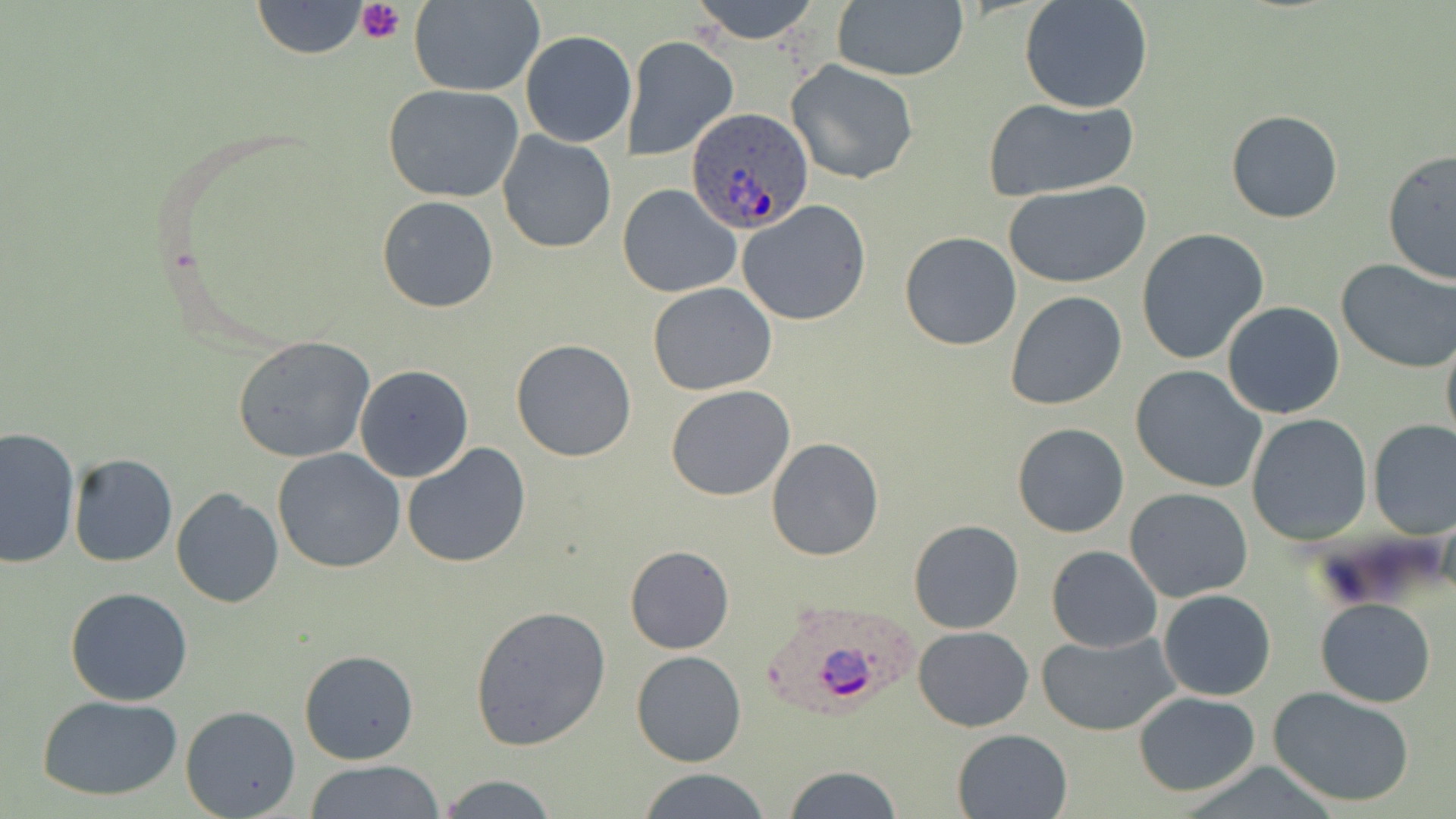

Summary:
  - Coordinate format: approximate bounding boxes as (x1,y1)-(x2,y2) corner pairs in pixels
  - Uninfected red blood cell locations: (252,0)-(369,59), (688,0)-(824,45), (830,0)-(969,82), (1019,0)-(1154,114), (409,1)-(545,96), (520,29)-(637,147), (621,37)-(738,160), (787,60)-(919,185), (382,85)-(524,204), (981,96)-(1140,201), (1226,108)-(1344,223), (496,131)-(617,255), (1382,150)-(1456,285), (1005,181)-(1150,288), (618,182)-(742,299), (376,195)-(500,313), (738,200)-(872,326), (1136,228)-(1271,365), (900,232)-(1020,351), (1336,257)-(1456,373), (648,282)-(778,394), (1004,290)-(1128,410), (1221,302)-(1345,418), (1440,333)-(1456,452), (233,336)-(374,463), (510,339)-(637,462), (354,364)-(473,481), (1131,365)-(1269,494), (665,384)-(795,501), (1245,413)-(1372,546), (1367,420)-(1455,537), (1012,423)-(1129,538), (0,426)-(80,568), (766,438)-(885,560), (402,443)-(532,569), (272,448)-(405,573), (68,454)-(178,568), (171,488)-(283,608), (1124,488)-(1254,602), (908,520)-(1024,635), (624,544)-(735,653), (1045,544)-(1162,652), (65,586)-(194,707), (1158,589)-(1276,702), (1315,599)-(1436,708), (470,604)-(612,750), (913,626)-(1034,731), (1038,631)-(1181,737), (299,648)-(420,766), (630,650)-(746,767), (1268,686)-(1417,807), (1131,689)-(1261,796), (36,693)-(187,802), (180,706)-(302,819), (952,728)-(1073,818), (304,761)-(447,817), (782,765)-(904,819), (634,768)-(771,819), (435,774)-(560,817)
  - Platelet locations: (356,0)-(404,44)
  - Plasmodium ovale-infected red blood cell locations: (685,109)-(813,235), (760,598)-(925,721)
  - Slide-level diagnosis: Plasmodium ovale
  - Modality: light microscopy
  - Field of view: single
  - Image size: 1456×819 pixels
  - Magnification: 1000x
  - Stain: May-Grünwald-Giemsa
  - Preparation: thin blood film